Comment on the morphology of the erythrocytes.
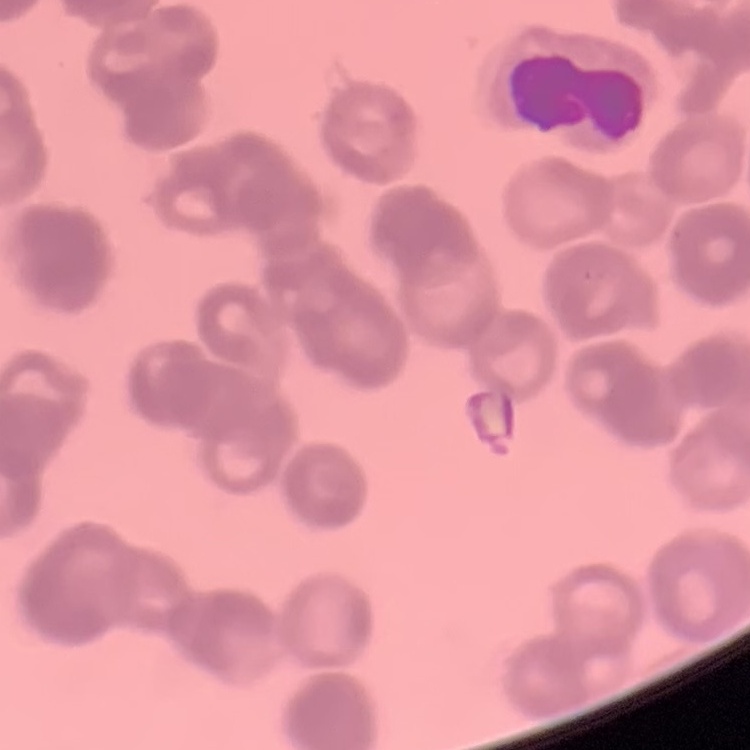

Rouleaux formation.

stain = Field's or Giemsa
image type = square crop of a larger photomicrograph
preparation = thin blood film